Name the blood parasite species.
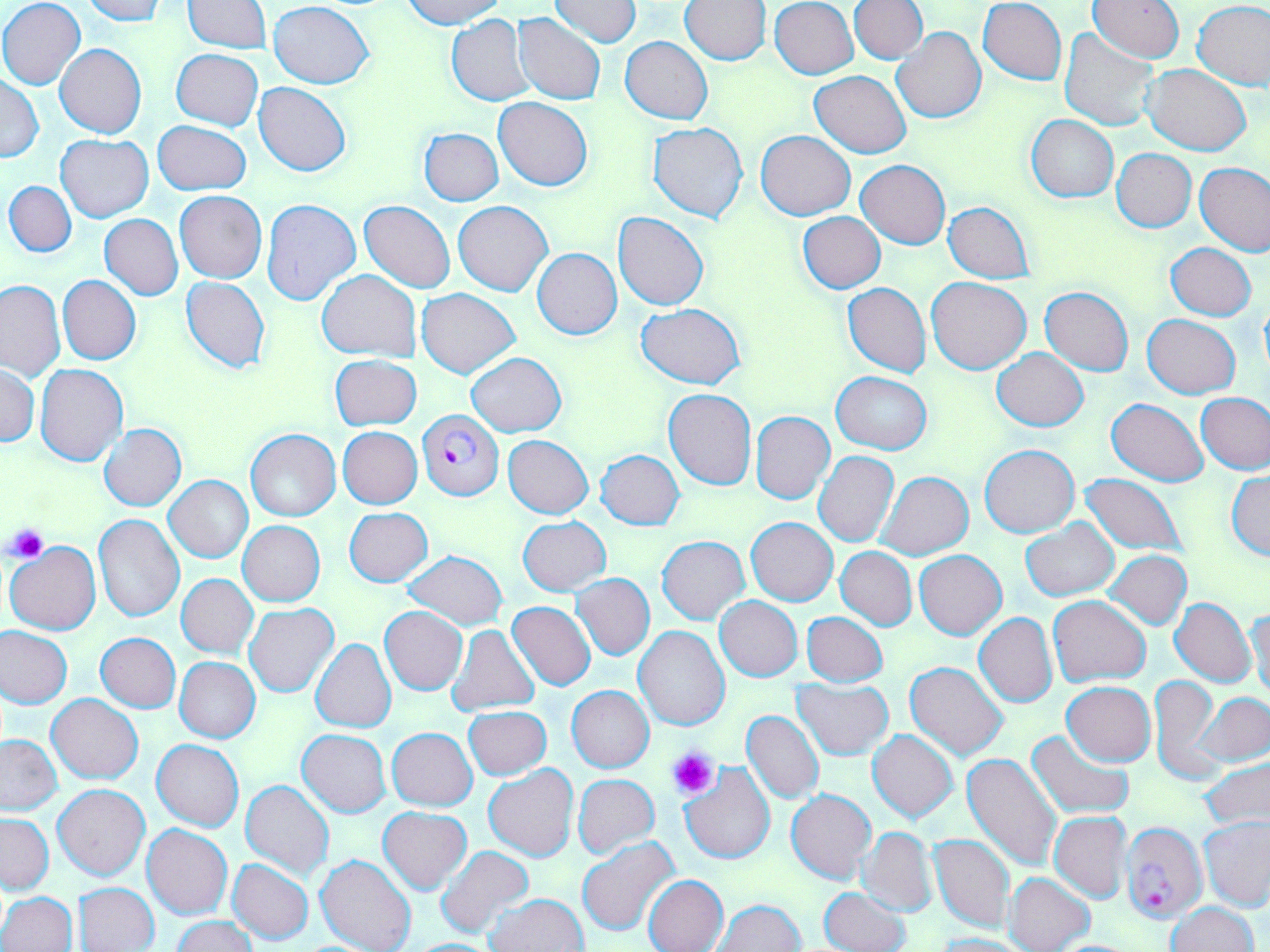

Plasmodium falciparum.

Approximate bounding boxes as [x1, y1, x2, y2] in pixels. Uninfected red blood cell locations (subset): [1, 0, 86, 90], [79, 0, 166, 23], [182, 0, 270, 52], [399, 0, 505, 27], [978, 0, 1066, 85], [1089, 0, 1183, 63], [550, 1, 641, 48], [680, 1, 770, 66], [769, 1, 858, 79], [848, 1, 928, 63], [269, 2, 373, 88], [1193, 2, 1270, 90], [513, 12, 607, 106], [447, 14, 536, 106], [893, 27, 986, 124], [1060, 28, 1158, 132], [621, 36, 713, 123], [55, 44, 147, 138], [170, 49, 264, 131], [1144, 64, 1251, 155], [810, 71, 910, 158], [0, 75, 42, 162], [254, 82, 351, 175], [494, 97, 592, 191], [1025, 115, 1118, 202], [153, 120, 250, 195], [648, 122, 749, 223], [418, 127, 504, 205], [755, 130, 855, 220], [55, 135, 154, 222], [1112, 149, 1196, 231], [856, 159, 950, 249], [1195, 164, 1270, 256], [4, 181, 77, 257], [175, 190, 266, 283], [261, 198, 362, 305], [360, 201, 454, 293], [454, 201, 553, 297], [944, 202, 1034, 283], [613, 212, 709, 310], [798, 212, 886, 293], [100, 214, 183, 300], [1166, 243, 1256, 320], [532, 248, 622, 340], [317, 270, 420, 360], [58, 276, 140, 366], [181, 276, 270, 373], [926, 276, 1031, 374], [0, 280, 65, 380], [844, 283, 930, 376], [1040, 286, 1133, 375], [417, 289, 519, 378], [1259, 296, 1270, 383], [637, 302, 744, 388], [1142, 314, 1241, 398], [992, 348, 1088, 431], [466, 353, 566, 436], [330, 355, 421, 430], [36, 365, 128, 466], [1, 366, 39, 445], [831, 371, 931, 454], [664, 388, 756, 490], [1196, 392, 1269, 475], [1106, 398, 1209, 486], [750, 410, 834, 503], [99, 423, 187, 511], [338, 427, 423, 509], [245, 428, 341, 521], [503, 435, 593, 518], [980, 444, 1079, 538], [596, 449, 684, 530], [814, 451, 900, 548], [1226, 470, 1270, 560], [875, 471, 974, 561], [1078, 471, 1188, 559], [165, 475, 253, 564], [344, 507, 432, 587], [94, 515, 183, 621], [518, 516, 610, 595], [746, 517, 837, 606], [1021, 518, 1118, 602], [238, 520, 325, 606], [657, 535, 749, 625], [5, 541, 101, 635], [836, 546, 916, 630], [915, 550, 1006, 639], [1105, 550, 1192, 630], [403, 551, 508, 628], [572, 574, 655, 660], [177, 575, 257, 658], [1048, 595, 1151, 688], [714, 596, 803, 682], [1170, 597, 1257, 687], [507, 601, 595, 691], [245, 604, 338, 697], [1246, 605, 1269, 701], [380, 607, 468, 694], [975, 609, 1145, 698], [801, 611, 888, 687], [974, 613, 1057, 708], [447, 625, 539, 715], [634, 625, 729, 731], [0, 626, 73, 710], [96, 632, 180, 712], [311, 639, 396, 733], [175, 657, 261, 743], [906, 662, 1009, 760], [1151, 676, 1222, 785], [791, 679, 894, 761], [1061, 682, 1155, 767], [566, 685, 654, 772], [1196, 691, 1270, 768], [47, 694, 143, 784], [463, 706, 551, 780], [741, 710, 825, 805], [387, 727, 477, 810], [297, 729, 390, 816], [867, 729, 958, 822], [1026, 729, 1134, 820], [0, 735, 63, 815], [152, 739, 243, 831], [961, 752, 1065, 871], [1200, 755, 1270, 830], [679, 763, 775, 863], [484, 765, 580, 863], [572, 774, 659, 860], [241, 780, 334, 880], [53, 783, 149, 880], [786, 788, 876, 885], [378, 807, 472, 893], [1049, 812, 1131, 902], [1, 813, 53, 893], [1199, 817, 1270, 910], [142, 825, 233, 920], [857, 827, 938, 916], [929, 833, 1014, 933], [577, 837, 680, 935], [437, 845, 534, 939], [315, 853, 417, 952], [229, 859, 314, 944], [1004, 872, 1095, 952], [644, 875, 728, 952], [75, 882, 159, 951], [818, 887, 910, 952], [1, 892, 77, 952], [485, 893, 588, 952], [711, 899, 804, 951], [1167, 902, 1258, 952], [173, 916, 258, 952], [931, 933, 1032, 952], [406, 938, 505, 951]. Plasmodium falciparum-infected red blood cell locations (subset): [417, 410, 504, 501]. Platelet locations: [6, 524, 49, 563], [668, 746, 721, 799]. Thin blood smear. May-Grünwald-Giemsa stain. Single field of view. Light microscopy. 1000x magnification. Image is 1270×952 pixels.